Classify this cell by malaria status.
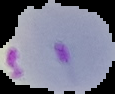
Parasitized.

image size = 115×94 pixels
preparation = thin blood film
image type = segmented cell region with the area outside set to black